Identify the blood parasite species.
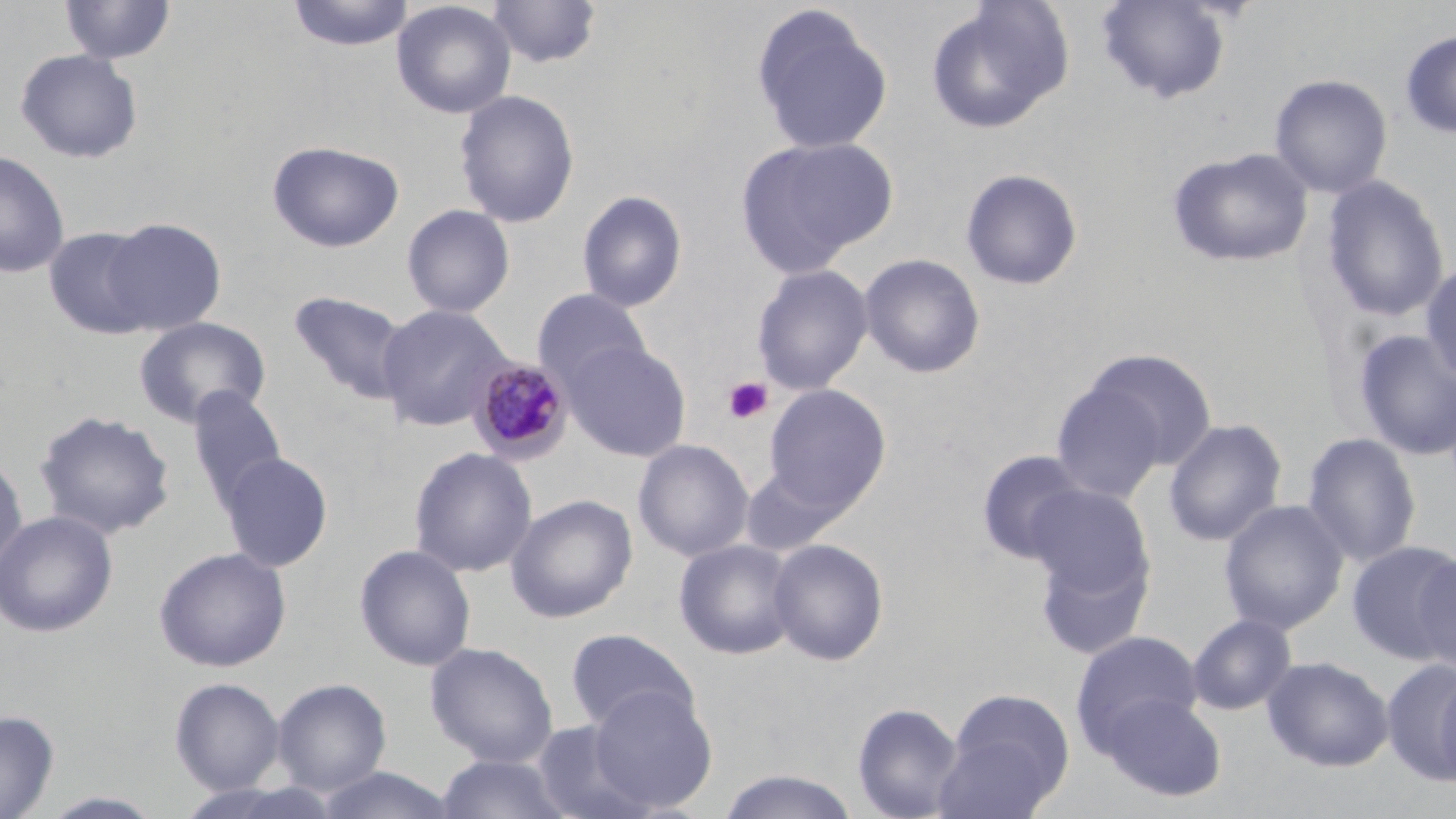

Plasmodium malariae.

Summary:
  - Coordinate format: approximate bounding boxes as (x1, y1, x2, y2) in pixels
  - Plasmodium malariae-infected red blood cell locations: (467, 357, 573, 464)
  - Platelet locations: (722, 376, 774, 425)
  - Uninfected red blood cell locations: (287, 0, 415, 51), (1095, 0, 1233, 105), (60, 1, 175, 66), (391, 1, 516, 119), (487, 1, 601, 69), (925, 1, 1074, 135), (750, 4, 894, 157), (1400, 30, 1456, 140), (14, 48, 144, 164), (1269, 73, 1392, 199), (454, 89, 579, 229), (734, 135, 898, 278), (267, 140, 405, 253), (1167, 147, 1315, 269), (0, 149, 70, 278), (960, 168, 1084, 291), (1320, 175, 1450, 323), (576, 190, 688, 313), (402, 204, 515, 318), (100, 218, 227, 334), (43, 226, 160, 340), (859, 253, 986, 379), (1420, 260, 1456, 387), (752, 264, 873, 396), (532, 289, 652, 397), (288, 290, 412, 406), (375, 304, 510, 432), (134, 316, 271, 428), (1351, 329, 1456, 461), (565, 341, 691, 461), (1078, 348, 1218, 474), (1049, 378, 1174, 503), (762, 384, 892, 517), (186, 386, 288, 514), (34, 410, 175, 540), (1163, 418, 1287, 547), (1301, 432, 1422, 568), (633, 439, 754, 562), (409, 446, 538, 578), (976, 449, 1090, 564), (0, 451, 27, 576), (219, 452, 333, 572), (739, 463, 847, 557), (1024, 482, 1155, 606), (505, 493, 638, 623), (1219, 499, 1349, 636), (0, 510, 117, 638), (1032, 537, 1155, 662), (673, 538, 800, 661), (767, 538, 889, 666), (1346, 540, 1456, 664), (354, 544, 476, 671), (153, 546, 291, 672), (1413, 550, 1456, 674), (1187, 613, 1297, 715), (565, 628, 698, 734), (1071, 631, 1205, 753), (425, 642, 558, 766), (1261, 656, 1394, 772), (1380, 658, 1456, 784), (1433, 664, 1456, 793), (169, 677, 285, 795), (271, 678, 392, 797), (587, 685, 718, 812), (936, 688, 1074, 817), (1097, 691, 1227, 802), (852, 702, 963, 819), (0, 710, 59, 818), (531, 719, 654, 819), (434, 754, 574, 819), (312, 766, 461, 819), (715, 769, 862, 819), (37, 790, 168, 818)
  - Field of view: single
  - Image size: 1456×819 pixels
  - Modality: optical microscopy
  - Stain: May-Grünwald-Giemsa
  - Magnification: 1000x
  - Preparation: thin blood film